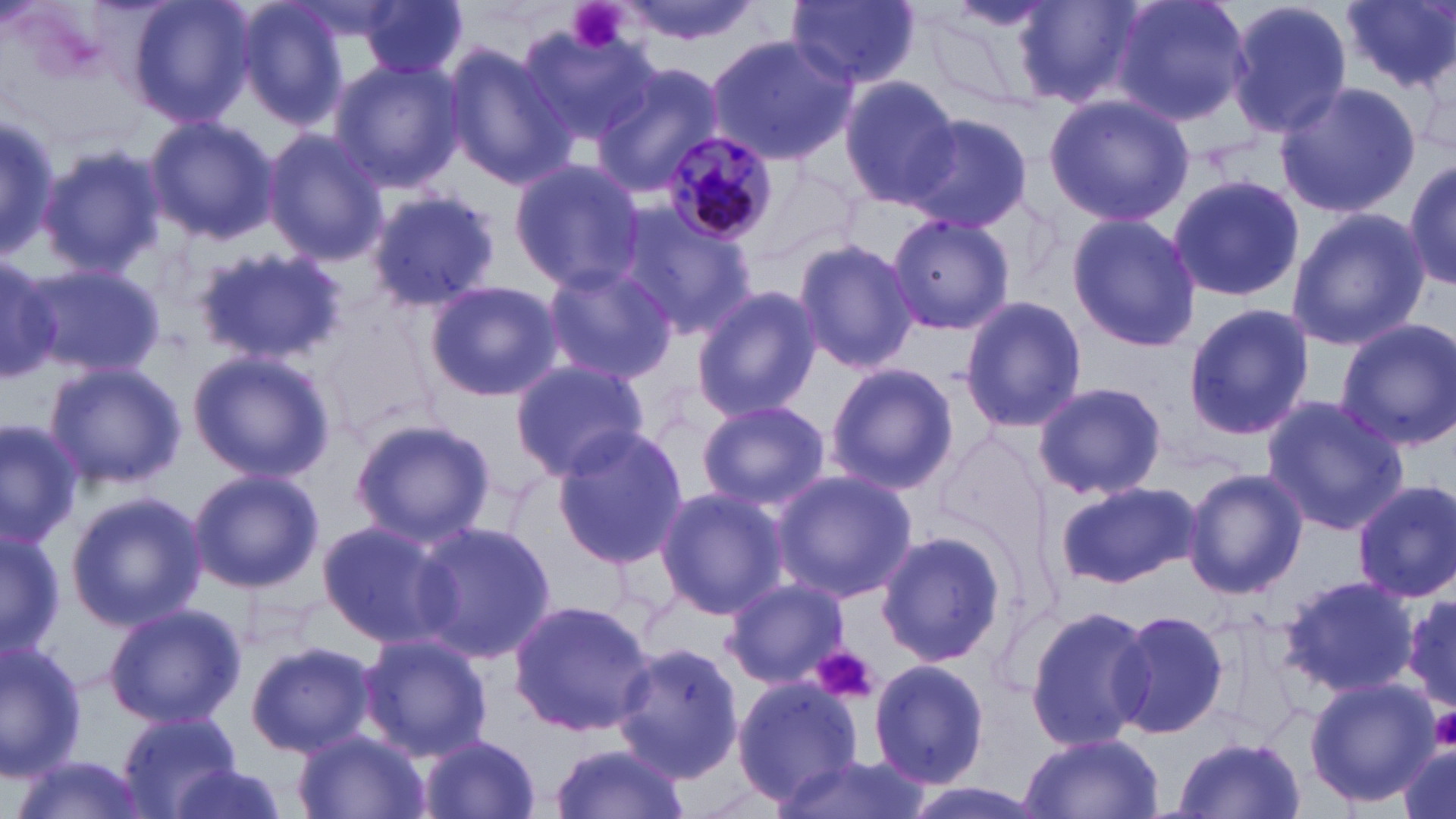
Summary:
  - Coordinate format: approximate bounding boxes as (x1,y1)-(x2,y2) corner pairs in pixels
  - Plasmodium malariae-infected red blood cell locations: (660,130)-(780,245)
  - Uninfected red blood cell locations: (127,0)-(257,129), (232,0)-(350,129), (356,0)-(468,79), (608,0)-(768,45), (786,0)-(922,89), (1108,0)-(1251,125), (1226,0)-(1354,140), (1340,0)-(1454,93), (1015,1)-(1142,107), (514,27)-(660,144), (705,35)-(857,164), (440,43)-(575,189), (328,58)-(462,194), (592,62)-(725,195), (838,78)-(959,207), (1275,82)-(1422,218), (1044,91)-(1193,227), (0,106)-(59,268), (144,114)-(276,244), (900,114)-(1032,232), (261,128)-(389,268), (34,143)-(164,280), (507,158)-(646,289), (1405,158)-(1456,291), (748,165)-(862,278), (1166,173)-(1308,304), (366,188)-(504,311), (614,205)-(755,341), (1284,207)-(1429,351), (1065,212)-(1202,352), (884,213)-(1016,337), (792,237)-(918,376), (194,247)-(344,365), (0,251)-(87,385), (22,261)-(165,384), (540,261)-(678,383), (425,279)-(561,401), (689,285)-(821,422), (960,297)-(1088,433), (1182,304)-(1316,440), (1335,318)-(1456,452), (187,349)-(335,483), (42,360)-(187,491), (511,360)-(653,481), (825,362)-(958,496), (1032,381)-(1167,500), (1261,395)-(1409,536), (696,398)-(832,514), (349,417)-(493,546), (0,420)-(82,550), (552,427)-(688,570), (1181,466)-(1308,600), (188,467)-(323,593), (769,468)-(917,603), (1056,479)-(1202,588), (1352,480)-(1456,602), (654,486)-(786,616), (65,490)-(205,632), (316,518)-(459,647), (412,519)-(555,662), (0,523)-(62,659), (875,529)-(1005,669), (1281,572)-(1419,698), (722,577)-(848,688), (1401,588)-(1456,717), (508,598)-(658,739), (104,601)-(246,730), (1023,602)-(1155,751), (1109,606)-(1233,741), (357,631)-(493,759), (0,638)-(86,778), (615,640)-(742,784), (246,642)-(377,757), (869,658)-(990,789), (729,676)-(862,803), (1304,677)-(1439,808), (117,711)-(241,818), (292,729)-(427,819), (1015,732)-(1166,819), (416,733)-(542,819), (1172,735)-(1309,819), (548,741)-(688,819), (1394,741)-(1456,819), (778,753)-(930,819), (9,757)-(155,819), (161,762)-(291,819)
  - Platelet locations: (565,0)-(630,54), (811,646)-(880,705), (1429,708)-(1456,749)
  - Slide-level diagnosis: Plasmodium malariae
  - Magnification: 1000x
  - Modality: light microscopy
  - Preparation: thin blood film
  - Field of view: one of a larger specimen
  - Image size: 1456×819 pixels
  - Stain: May-Grünwald-Giemsa